Name the parasite shown.
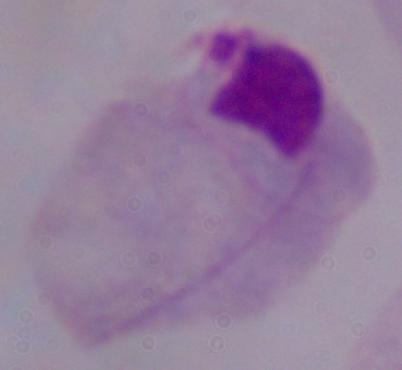
This is a trichomonad.

1000x magnification. Photomicrograph.